Identify the parasite.
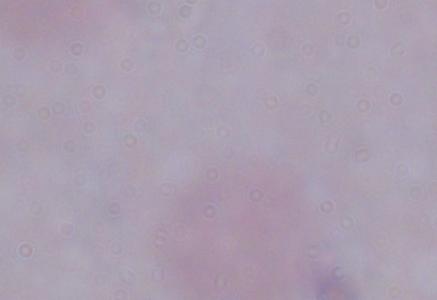

This is a trypanosome.

Captured at 1000x magnification. Photomicrograph.